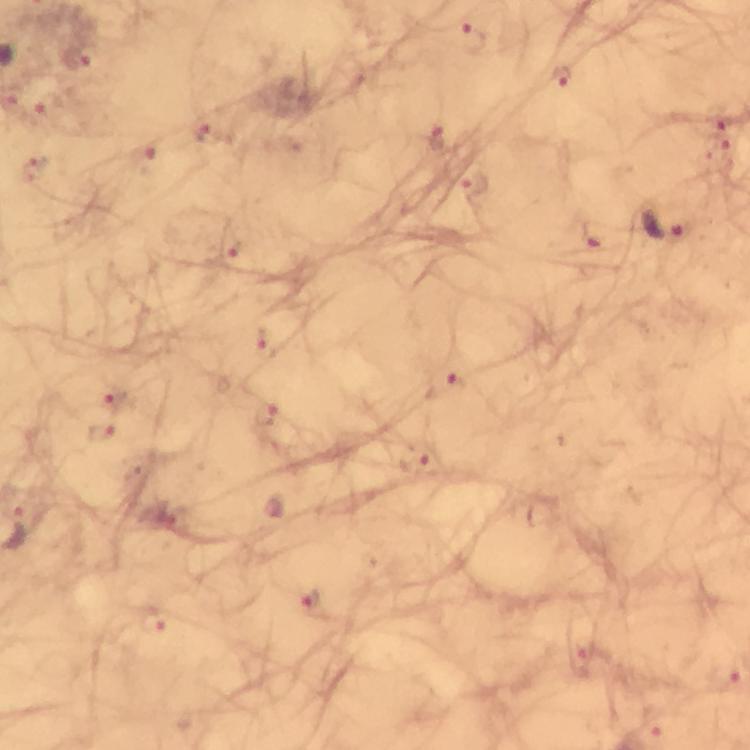
Approximate centers as [x, y] in pixels. Plasmodium parasite locations: [473, 38], [78, 59], [561, 78], [49, 105], [718, 123], [210, 134], [438, 136], [716, 150], [142, 158], [33, 171], [474, 185], [663, 223], [591, 239], [234, 247], [263, 339], [446, 385], [114, 399], [265, 414], [102, 432], [415, 459], [15, 529], [312, 602], [153, 621], [584, 661]. Thick blood film. At 100x magnification. A crop from one field of view. Photographed with a smartphone mounted on the microscope. Immersion oil was used. From a diagnostic examination for malaria. Giemsa-stained preparation. Image is 750×750 pixels.